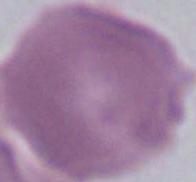
{
  "identification": "erythrocyte",
  "magnification": "1000x",
  "modality": "micrograph"
}